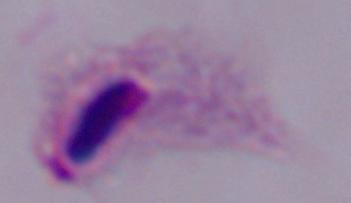

Summary:
  - Identification: trichomonad
  - Modality: micrograph
  - Magnification: 1000x